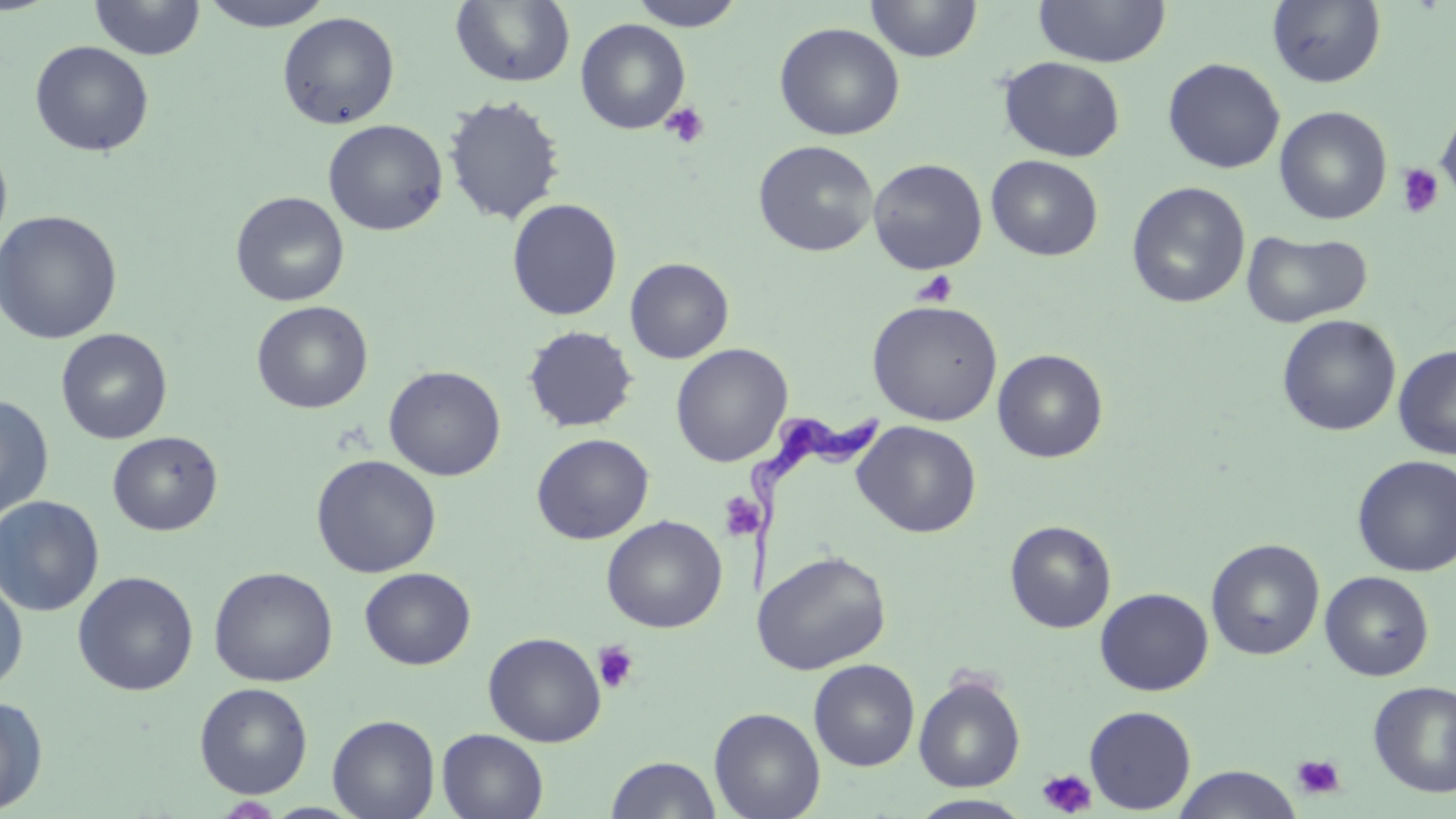
slide-level diagnosis = Trypanosoma brucei
magnification = 1000x
uninfected red blood cell locations = approximate bounding boxes as named x1/y1/x2/y2 corners in pixels: (x1=89, y1=0, x2=205, y2=61), (x1=200, y1=0, x2=334, y2=32), (x1=451, y1=0, x2=575, y2=87), (x1=628, y1=0, x2=747, y2=31), (x1=865, y1=0, x2=982, y2=63), (x1=1033, y1=0, x2=1171, y2=67), (x1=1266, y1=0, x2=1387, y2=88), (x1=277, y1=12, x2=400, y2=130), (x1=575, y1=19, x2=690, y2=134), (x1=774, y1=22, x2=904, y2=141), (x1=29, y1=40, x2=155, y2=157), (x1=998, y1=56, x2=1126, y2=162), (x1=1163, y1=58, x2=1285, y2=174), (x1=442, y1=94, x2=566, y2=226), (x1=1274, y1=105, x2=1393, y2=225), (x1=1436, y1=105, x2=1456, y2=206), (x1=322, y1=119, x2=448, y2=236), (x1=0, y1=139, x2=13, y2=255), (x1=753, y1=140, x2=879, y2=257), (x1=986, y1=155, x2=1103, y2=261), (x1=867, y1=158, x2=987, y2=274), (x1=1126, y1=182, x2=1250, y2=309), (x1=230, y1=191, x2=349, y2=306), (x1=506, y1=197, x2=623, y2=321), (x1=0, y1=210, x2=122, y2=345), (x1=1241, y1=229, x2=1372, y2=328), (x1=625, y1=258, x2=734, y2=363), (x1=867, y1=299, x2=1003, y2=426), (x1=251, y1=300, x2=373, y2=414), (x1=1277, y1=314, x2=1401, y2=436), (x1=522, y1=324, x2=639, y2=433), (x1=55, y1=328, x2=173, y2=444), (x1=670, y1=343, x2=793, y2=467), (x1=1394, y1=344, x2=1456, y2=460), (x1=992, y1=349, x2=1108, y2=463), (x1=383, y1=365, x2=506, y2=481), (x1=0, y1=394, x2=54, y2=521), (x1=852, y1=420, x2=981, y2=538), (x1=107, y1=431, x2=223, y2=535), (x1=531, y1=433, x2=654, y2=544), (x1=310, y1=454, x2=442, y2=578), (x1=1352, y1=455, x2=1456, y2=577), (x1=0, y1=495, x2=105, y2=617), (x1=602, y1=515, x2=727, y2=633), (x1=1004, y1=520, x2=1116, y2=633), (x1=1206, y1=538, x2=1325, y2=661), (x1=754, y1=550, x2=891, y2=674), (x1=208, y1=566, x2=338, y2=687), (x1=359, y1=567, x2=475, y2=670), (x1=72, y1=570, x2=199, y2=695), (x1=1320, y1=571, x2=1434, y2=681), (x1=0, y1=574, x2=29, y2=694), (x1=1095, y1=588, x2=1214, y2=696), (x1=483, y1=631, x2=606, y2=747), (x1=808, y1=659, x2=921, y2=771), (x1=913, y1=673, x2=1026, y2=792), (x1=1368, y1=680, x2=1456, y2=797), (x1=194, y1=682, x2=313, y2=799), (x1=0, y1=695, x2=49, y2=815), (x1=1084, y1=705, x2=1197, y2=813), (x1=708, y1=707, x2=826, y2=819), (x1=327, y1=714, x2=440, y2=819), (x1=436, y1=728, x2=550, y2=819), (x1=605, y1=755, x2=722, y2=818), (x1=1173, y1=765, x2=1301, y2=819), (x1=909, y1=794, x2=1035, y2=818), (x1=214, y1=796, x2=283, y2=817)
image size = 1456×819 pixels
stain = May-Grünwald-Giemsa
Trypanosoma brucei locations = approximate bounding boxes as named x1/y1/x2/y2 corners in pixels: (x1=734, y1=406, x2=885, y2=605)
field of view = one of a larger specimen
preparation = thin blood film
modality = light microscopy
platelet locations = approximate bounding boxes as named x1/y1/x2/y2 corners in pixels: (x1=660, y1=102, x2=710, y2=149), (x1=1397, y1=164, x2=1444, y2=219), (x1=911, y1=270, x2=958, y2=308), (x1=718, y1=493, x2=763, y2=541), (x1=593, y1=640, x2=639, y2=694), (x1=1292, y1=753, x2=1345, y2=800), (x1=1036, y1=768, x2=1097, y2=817)